Classify this cell by malaria status.
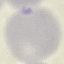
It is uninfected.

{
  "capture": "smartphone camera at the microscope eyepiece",
  "preparation": "thin blood smear",
  "image_type": "cell patch, automatically extracted from a larger field of view and resized to 64 × 64 pixels",
  "stain": "Giemsa"
}